Assess this cell for malaria.
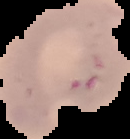

Parasitized.

preparation = thin blood film
image size = 130×139 pixels
image type = segmented cell region with the area outside set to black